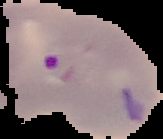 From a thin blood film. Image is 163×139 pixels. Segmented cell region on a black background. Result: malaria parasites identified.